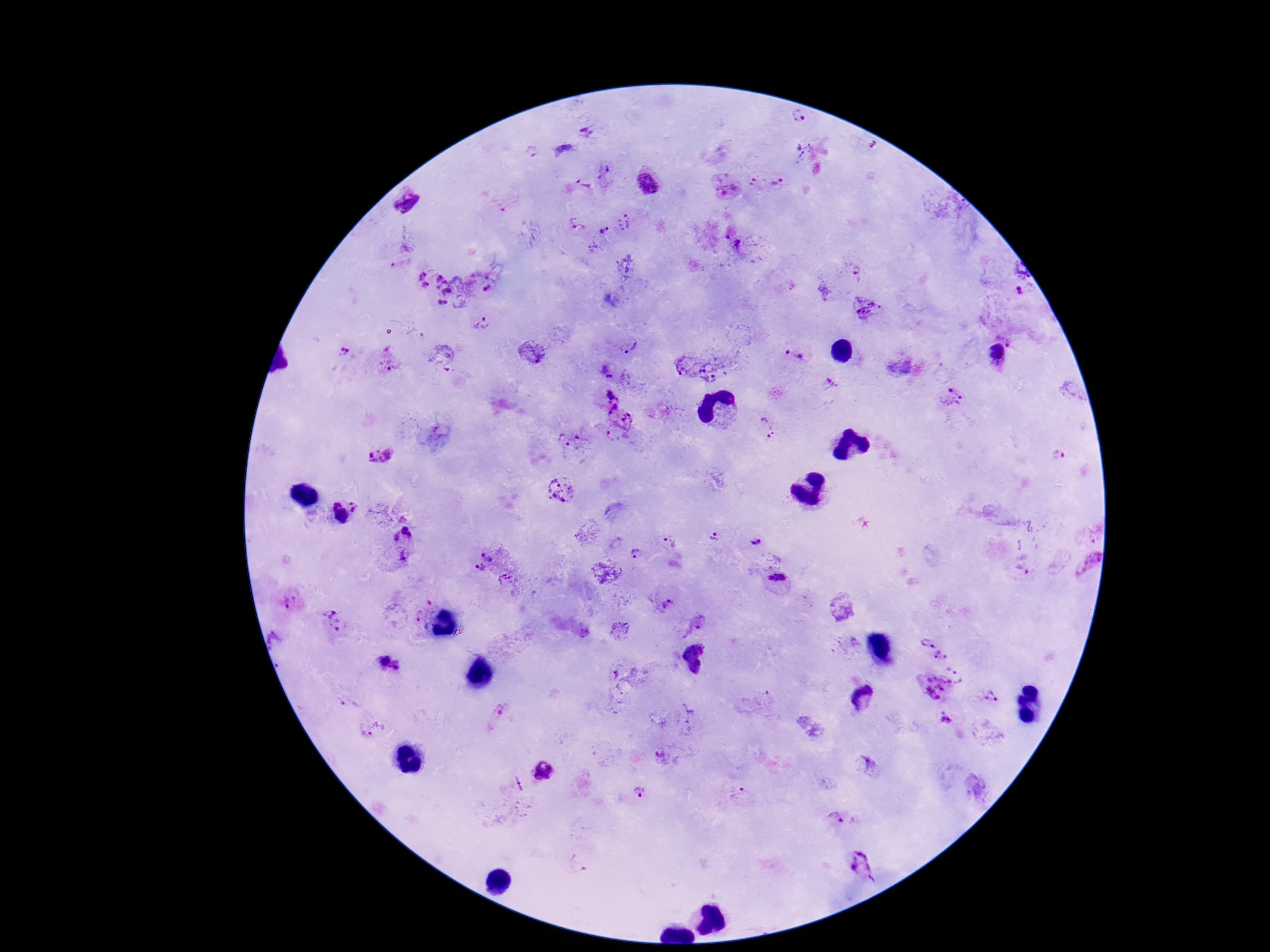

Approximate centers as [x, y] in pixels. Plasmodium parasite locations: [798, 116], [610, 172], [650, 181], [778, 182], [751, 184], [727, 185], [580, 186], [628, 221], [578, 226], [606, 230], [741, 246], [1015, 279], [486, 282], [435, 285], [868, 309], [481, 322], [630, 344], [341, 353], [999, 354], [794, 357], [388, 358], [684, 363], [713, 374], [611, 394], [954, 399], [618, 419], [767, 427], [573, 440], [1058, 454], [378, 455], [563, 488], [335, 502], [355, 505], [408, 531], [714, 536], [756, 540], [670, 543], [636, 553], [489, 555], [403, 557], [479, 569], [506, 578], [779, 578], [290, 603], [665, 605], [335, 622], [697, 624], [926, 641], [942, 654], [389, 665], [954, 666], [933, 688], [991, 692], [348, 705], [497, 715], [946, 720], [371, 728], [661, 757], [863, 764], [543, 772], [514, 783], [641, 793], [738, 793], [835, 817], [579, 864], [862, 865]. One field from this slide. Patient malaria status: positive. Giemsa-stained preparation. Image is 1270×952 pixels. Thick peripheral-blood smear. Smartphone photograph taken through the microscope eyepiece. 100x magnification.